Outline each blood parasite and name the species.
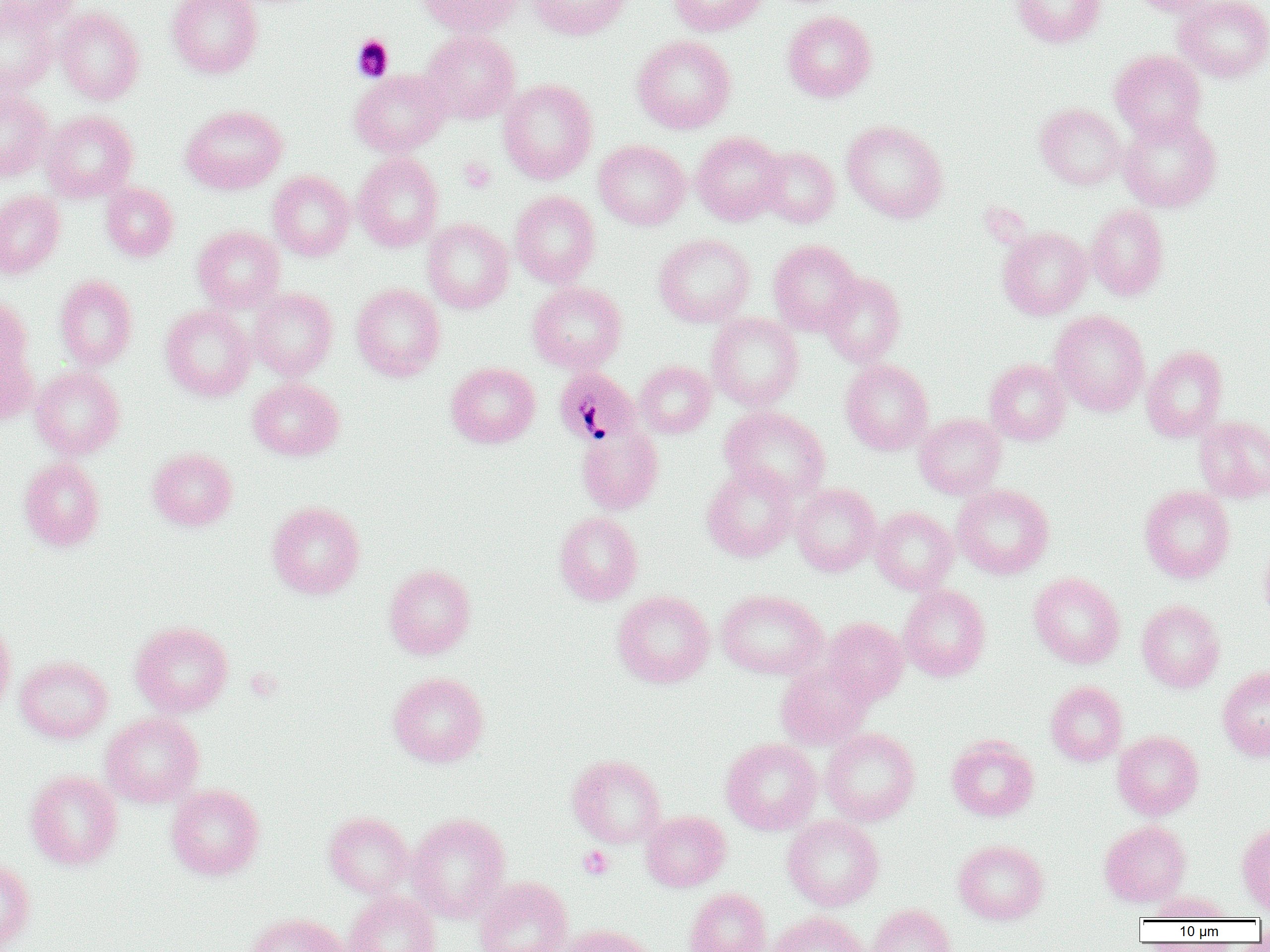

Approximate bounding boxes as (x1,y1)-(x2,y2) corner pairs in pixels.
Plasmodium malariae-infected red blood cells: (554,367)-(641,448).
No Plasmodium falciparum, Plasmodium ovale, Plasmodium vivax, Babesia divergens, or Trypanosoma brucei observed.

Uninfected red blood cell locations: (0,0)-(79,33), (167,0)-(263,78), (418,0)-(522,37), (527,0)-(633,40), (669,0)-(767,36), (1010,0)-(1107,47), (1128,0)-(1221,17), (1174,0)-(1270,82), (0,3)-(56,96), (54,6)-(145,104), (782,10)-(877,102), (421,30)-(520,123), (632,35)-(736,134), (1109,50)-(1206,141), (350,69)-(450,157), (498,78)-(598,184), (0,88)-(52,181), (1035,103)-(1126,189), (181,104)-(287,194), (41,110)-(138,202), (1118,112)-(1221,212), (842,120)-(949,223), (692,132)-(786,225), (594,139)-(690,230), (758,146)-(840,227), (353,153)-(444,252), (268,171)-(355,261), (101,183)-(179,262), (0,190)-(65,278), (510,191)-(600,288), (1086,204)-(1169,301), (422,218)-(514,313), (193,225)-(284,312), (998,227)-(1093,320), (654,233)-(756,328), (768,239)-(862,335), (820,272)-(906,367), (55,275)-(137,369), (527,282)-(627,373), (351,283)-(445,381), (248,288)-(337,380), (0,299)-(38,423), (160,305)-(255,401), (1050,310)-(1150,416), (706,313)-(804,410), (1141,346)-(1228,442), (985,358)-(1071,445), (840,359)-(933,455), (634,361)-(716,438), (446,362)-(541,448), (31,365)-(125,459), (248,377)-(344,461), (720,406)-(830,500), (914,413)-(1006,498), (1194,416)-(1270,503), (577,425)-(664,515), (147,448)-(237,531), (19,458)-(105,552), (701,464)-(798,562), (790,483)-(881,576), (953,484)-(1054,579), (1139,485)-(1235,583), (267,501)-(365,599), (871,507)-(958,595), (554,512)-(643,605), (1258,541)-(1270,627), (384,564)-(476,659), (1028,572)-(1125,668), (899,585)-(991,682), (612,590)-(714,688), (717,590)-(827,680), (1137,599)-(1225,692), (0,617)-(15,718), (821,617)-(908,704), (130,621)-(233,717), (15,656)-(113,743), (776,660)-(874,750), (1218,666)-(1270,761), (388,671)-(489,767), (1045,680)-(1128,766), (101,713)-(204,807), (820,727)-(920,826), (1112,730)-(1203,820), (946,734)-(1039,821), (721,738)-(822,835), (567,754)-(666,848), (25,769)-(123,870), (166,784)-(265,880), (640,810)-(731,891), (323,811)-(414,899), (405,813)-(510,923), (782,816)-(884,911), (1099,820)-(1191,906), (1236,821)-(1270,915), (953,839)-(1048,924), (0,857)-(36,951), (473,876)-(572,952), (684,887)-(771,952), (343,891)-(441,952), (1150,891)-(1234,921), (868,904)-(956,952), (767,911)-(869,952), (243,912)-(348,952), (556,924)-(659,952). Platelet locations: (351,35)-(394,81), (459,157)-(495,192), (578,845)-(614,880). Slide-level diagnosis: Plasmodium malariae. Single field of view. Light microscopy. Thin blood film. 1000x magnification. Image is 1270×952 pixels.